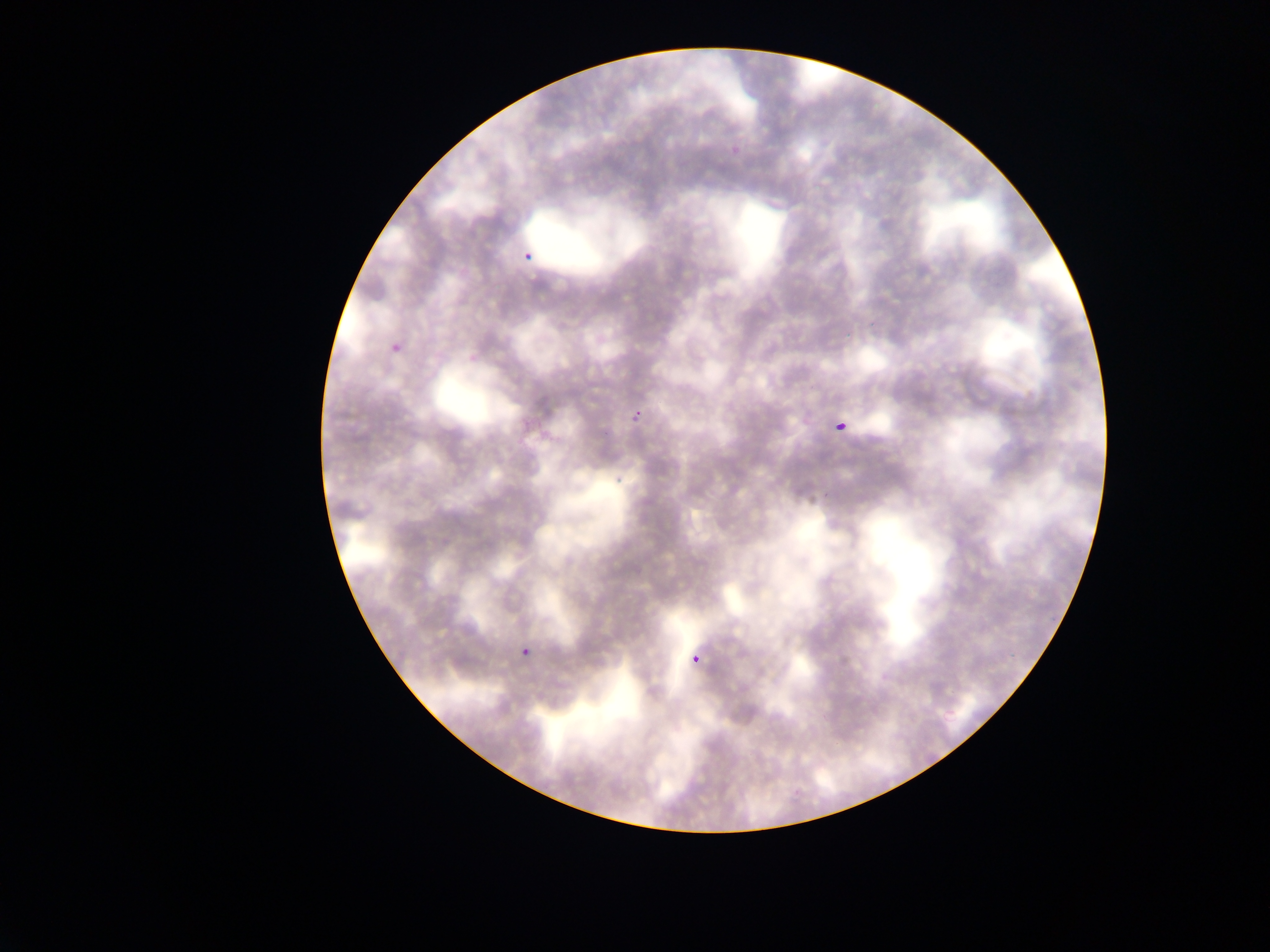
{
  "field_of_view": "single",
  "image_size": "1270×952 pixels",
  "country": "Ghana",
  "preparation": "thin blood film",
  "malaria_parasite_locations": "approximate bounding boxes as [left, top, right, bottom] in pixels: [519, 236, 539, 274], [382, 336, 397, 354], [622, 402, 647, 428], [832, 408, 855, 439], [513, 640, 533, 670], [683, 643, 704, 669]",
  "capture": "mobile-phone photograph through a microscope"
}